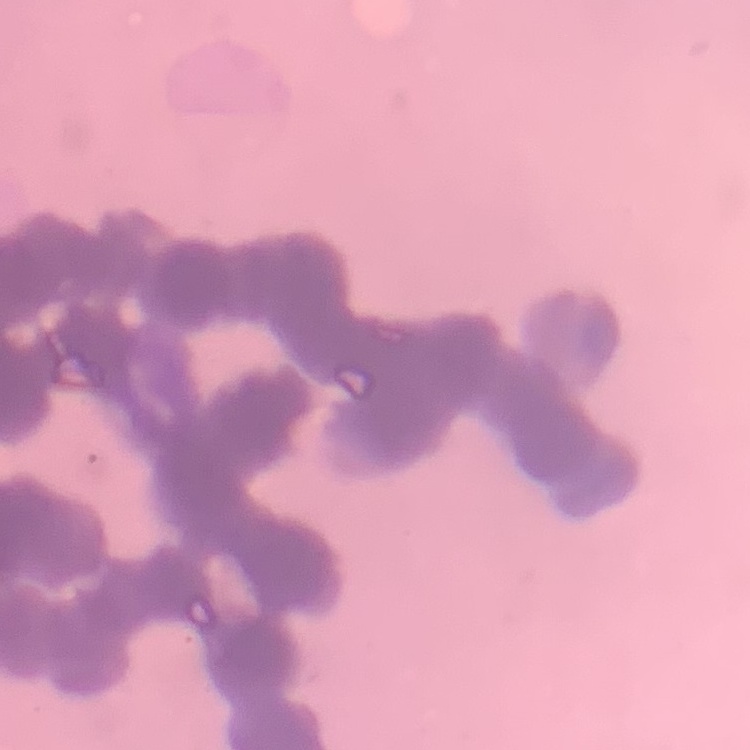

The red blood cells show rouleaux formation. Thin peripheral smear. Square crop of a larger photomicrograph. Stained with either Field's or Giemsa.